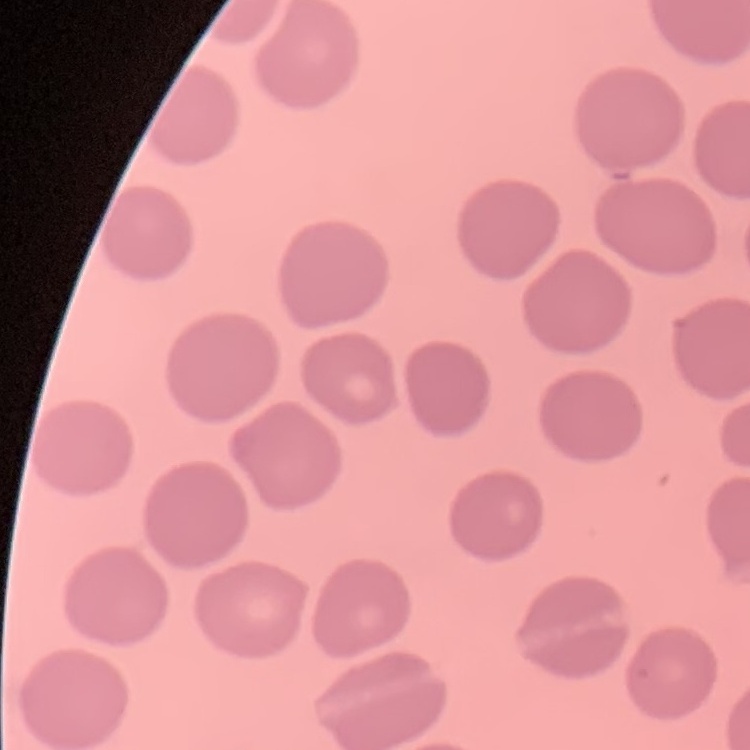
Summary:
  - Red blood cell morphology: no rouleaux formation
  - Stain: Field's or Giemsa
  - Image type: square crop of a larger photomicrograph
  - Preparation: thin blood smear